Assess this cell for malaria.
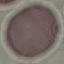
It is uninfected.

preparation = thin blood smear
capture = smartphone through the microscope eyepiece
image type = automatically extracted cell patch, resized to 64 × 64 pixels
stain = Giemsa